Name the blood parasite species.
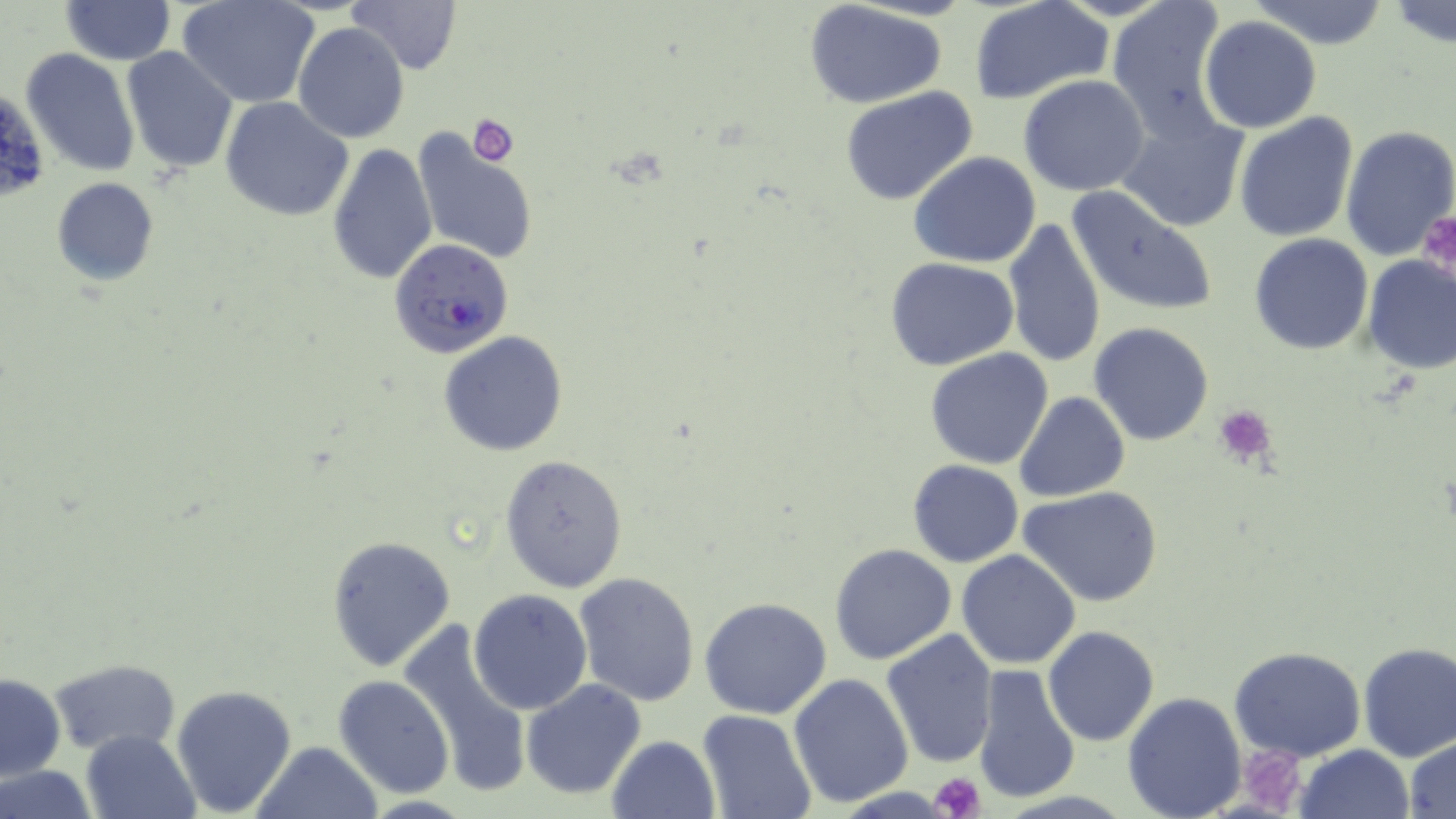
Plasmodium falciparum.

Approximate bounding boxes as (x1,y1)-(x2,y2) corner pairs in pixels. Plasmodium falciparum-infected red blood cell locations: (390,238)-(515,359). Uninfected red blood cell locations: (348,0)-(463,75), (1106,0)-(1233,140), (1250,0)-(1392,49), (60,1)-(175,65), (178,1)-(320,108), (970,1)-(1114,104), (803,2)-(950,109), (1386,2)-(1456,50), (1198,14)-(1324,133), (293,21)-(410,145), (120,46)-(238,174), (19,49)-(140,177), (1018,74)-(1151,194), (840,87)-(981,207), (0,89)-(48,208), (221,96)-(353,223), (1119,111)-(1249,233), (1234,113)-(1360,243), (1341,124)-(1456,260), (409,130)-(539,264), (327,143)-(438,288), (908,152)-(1042,270), (50,178)-(160,287), (1067,187)-(1218,317), (1001,218)-(1108,368), (1249,233)-(1374,355), (1361,254)-(1455,374), (885,257)-(1019,369), (1088,322)-(1216,446), (439,331)-(568,457), (925,347)-(1055,469), (1015,391)-(1130,502), (500,454)-(628,592), (907,459)-(1026,568), (1020,487)-(1167,608), (325,534)-(455,670), (830,543)-(958,664), (956,549)-(1081,670), (573,570)-(702,706), (468,589)-(594,715), (699,597)-(833,719), (396,620)-(534,796), (1043,627)-(1159,746), (880,628)-(998,766), (1357,643)-(1456,762), (1228,647)-(1367,761), (49,657)-(181,757), (971,664)-(1082,804), (1,673)-(64,781), (787,673)-(916,809), (333,675)-(454,797), (521,677)-(646,801), (170,682)-(298,817), (1122,691)-(1247,819), (696,708)-(817,819), (80,731)-(200,819), (606,735)-(722,819), (1406,738)-(1456,817), (250,741)-(384,819), (1297,744)-(1413,819), (0,765)-(100,819). Platelet locations: (467,114)-(522,166), (1425,216)-(1456,280), (1214,403)-(1278,465), (1243,747)-(1307,814), (929,772)-(988,819). Single field of view. Image is 1456×819 pixels. Thin blood film. Light microscopy. 1000x magnification. May-Grünwald-Giemsa stain.